Locate every Plasmodium malariae-infected red blood cell.
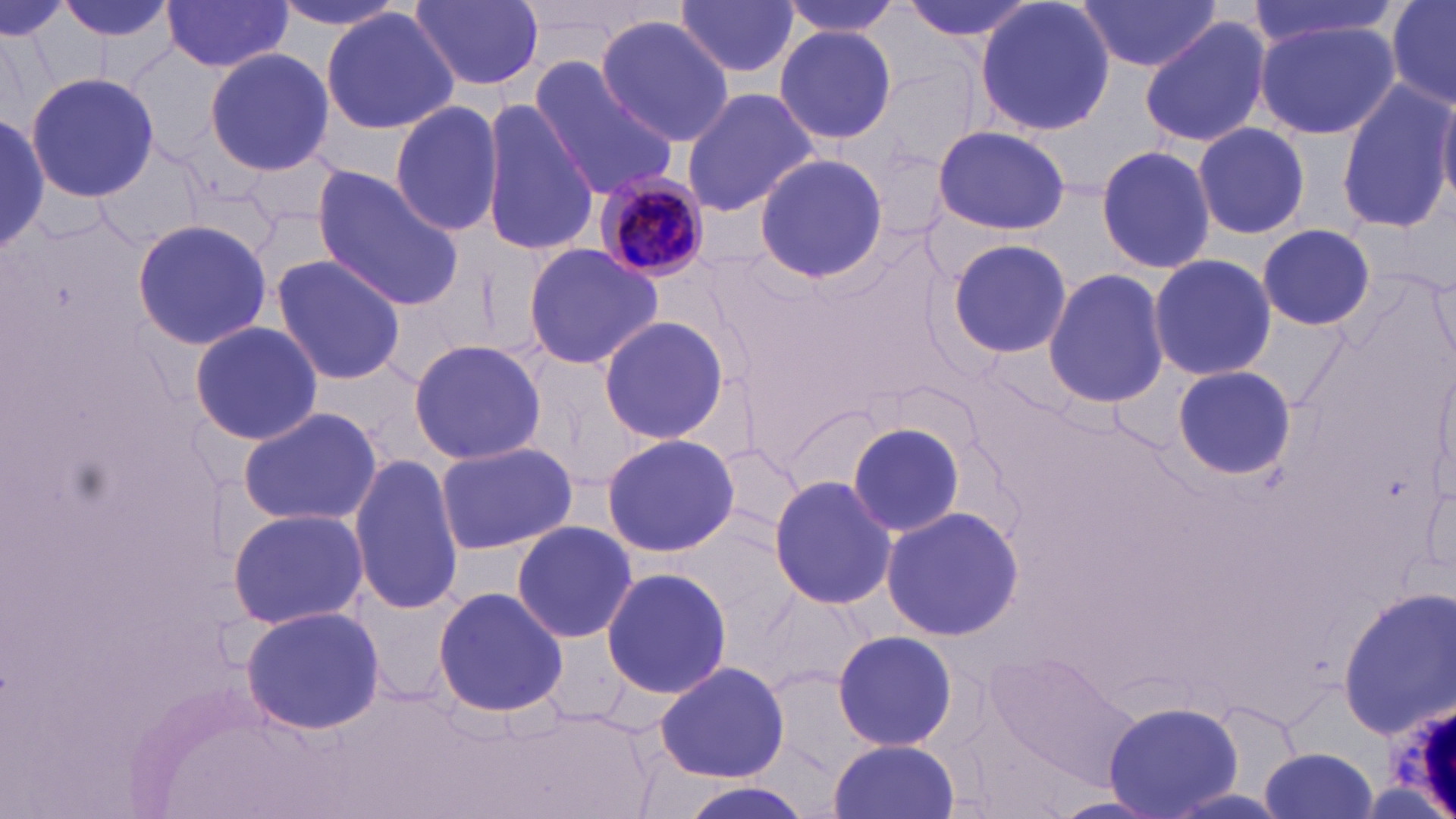

Approximate bounding boxes as (x1, y1, x2, y2) in pixels.
Plasmodium malariae-infected red blood cells: (590, 173, 713, 281).

slide-level diagnosis = Plasmodium malariae
image size = 1456×819 pixels
preparation = thin blood film
uninfected red blood cell locations = approximate bounding boxes as (x1, y1, x2, y2) in pixels: (49, 0, 179, 46), (266, 0, 421, 33), (408, 0, 546, 94), (778, 0, 906, 38), (897, 0, 1038, 46), (974, 0, 1115, 138), (1075, 0, 1220, 74), (1244, 0, 1403, 50), (1384, 0, 1456, 110), (675, 1, 802, 79), (161, 3, 293, 77), (321, 8, 458, 136), (595, 15, 737, 144), (1139, 15, 1272, 148), (1255, 20, 1397, 139), (773, 25, 899, 145), (203, 47, 335, 175), (527, 59, 679, 200), (26, 72, 158, 205), (1335, 78, 1453, 233), (678, 87, 820, 215), (1435, 88, 1456, 207), (389, 99, 507, 238), (478, 99, 596, 260), (0, 110, 50, 252), (1193, 121, 1311, 240), (932, 125, 1069, 235), (1095, 143, 1214, 275), (752, 152, 888, 285), (310, 168, 464, 310), (131, 218, 272, 352), (1257, 223, 1376, 331), (944, 239, 1071, 359), (521, 244, 664, 370), (1146, 253, 1277, 384), (269, 255, 408, 386), (1043, 266, 1169, 409), (1430, 266, 1454, 363), (595, 314, 734, 448), (190, 320, 325, 446), (408, 339, 548, 464), (1170, 365, 1295, 479), (1436, 365, 1456, 498), (238, 406, 382, 530), (844, 420, 967, 537), (599, 431, 739, 558), (433, 440, 578, 555), (349, 454, 466, 613), (769, 474, 897, 611), (878, 504, 1024, 642), (228, 506, 369, 629), (510, 520, 637, 645), (600, 566, 733, 699), (433, 586, 569, 718), (1339, 588, 1455, 736), (239, 605, 386, 736), (831, 629, 958, 752), (987, 648, 1141, 783), (656, 660, 789, 783), (1103, 701, 1242, 818), (828, 738, 961, 818), (1262, 747, 1378, 819)
magnification = 1000x
field of view = one of a larger specimen
stain = May-Grünwald-Giemsa
modality = optical microscopy